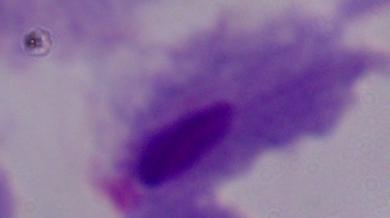
Photomicrograph. A trichomonad is seen. Captured at 1000x magnification.